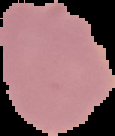

Summary:
  - Image size: 115×136 pixels
  - Image type: segmented cell region on a black background
  - Malaria status: uninfected
  - Preparation: thin blood film